Assess this cell for malaria.
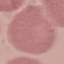
It is uninfected.

stain = Giemsa
preparation = thin blood smear
capture = smartphone camera at the microscope eyepiece
image type = automatically extracted cell patch, resized to 64 × 64 pixels